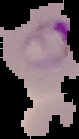

Summary:
  - Image size: 79×139 pixels
  - Malaria status: parasitized
  - Image type: cell region segmented out of the field of view; surrounding area masked to black
  - Preparation: thin blood film